Classify this cell by malaria status.
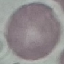

It is uninfected.

Photographed with a smartphone camera at the microscope eyepiece. Giemsa stain. Cell patch, automatically extracted from a larger field of view and resized to 64 × 64 pixels. Thin blood smear.